Describe the morphology of the erythrocytes.
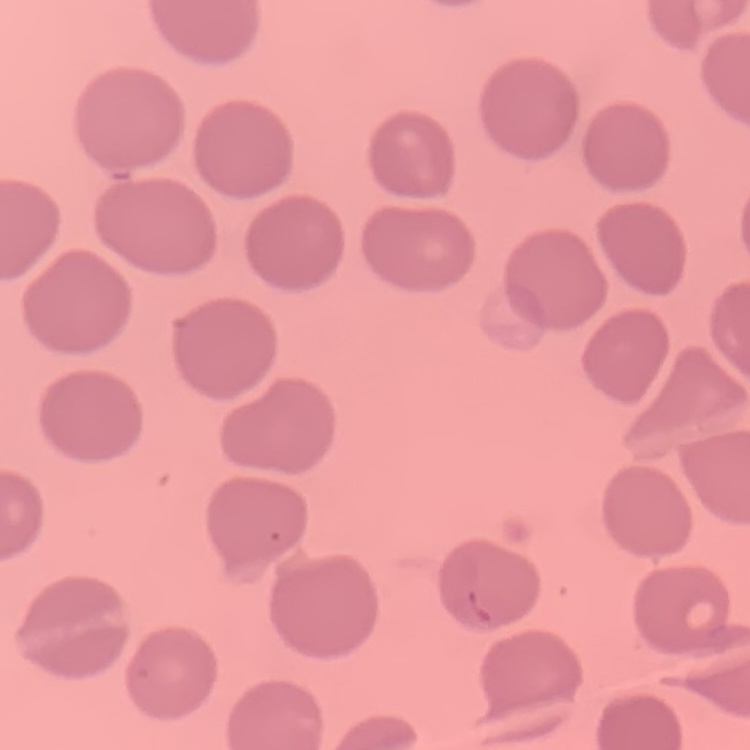
No rouleaux formation.

Field's or Giemsa stain. Thin blood smear. Square crop of a larger photomicrograph.